Comment on the morphology of the red blood cells.
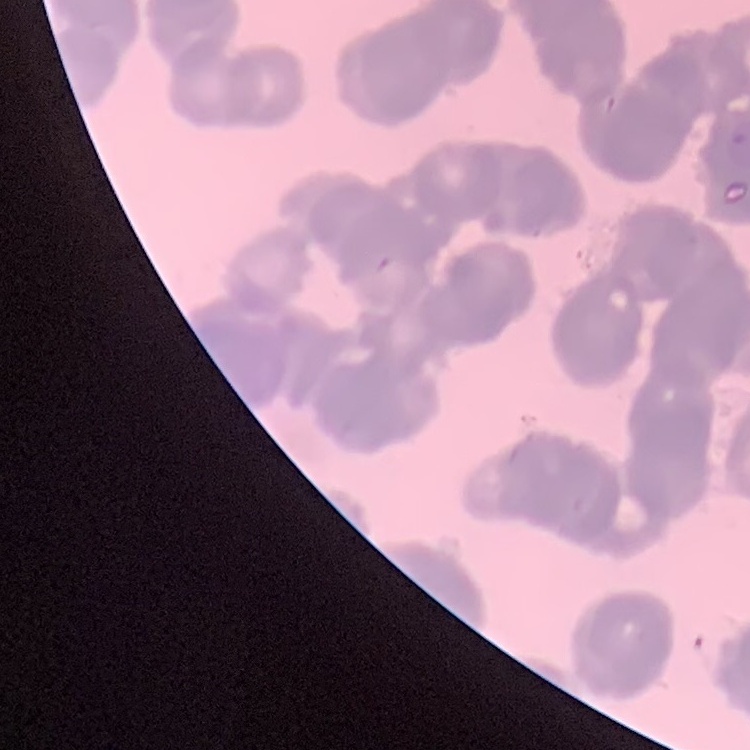

They show rouleaux formation.

image type = one tile cut from a larger photomicrograph
stain = Field's or Giemsa
preparation = thin peripheral smear